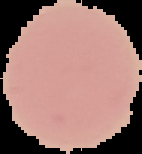
Summary:
  - Malaria status: uninfected
  - Image type: cell region segmented out of the field of view; surrounding area masked to black
  - Image size: 142×154 pixels
  - Preparation: thin blood smear